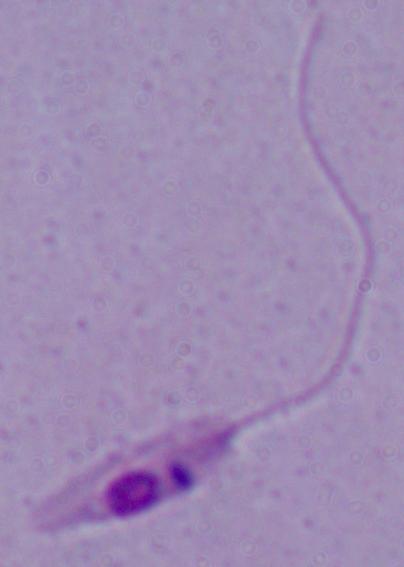
{
  "modality": "photomicrograph",
  "identification": "Leishmania",
  "magnification": "1000x"
}